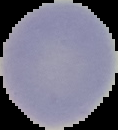
{
  "image_type": "cell region segmented out of the field of view; surrounding area masked to black",
  "malaria_status": "uninfected",
  "image_size": "118×130 pixels",
  "preparation": "thin blood film"
}